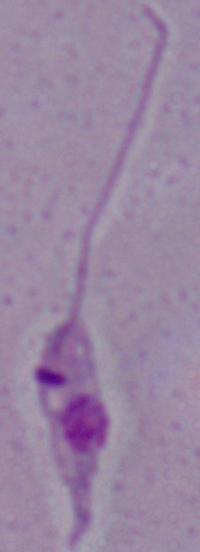 Photomicrograph. A Leishmania parasite is seen. 1000x magnification.